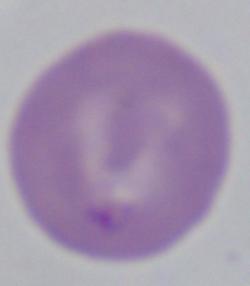 A Babesia parasite is shown. 1000x magnification. Photomicrograph.